Report the malaria status of this cell.
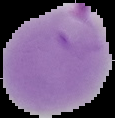

Parasitized.

From a thin blood film. The area outside the segmented cell region is set to black. Image is 115×118 pixels.